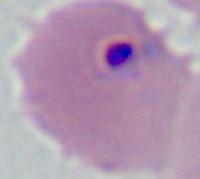
Summary:
  - Identification: Plasmodium
  - Magnification: 400x or 1000x
  - Modality: photomicrograph